Point out malaria parasites and leukocytes.
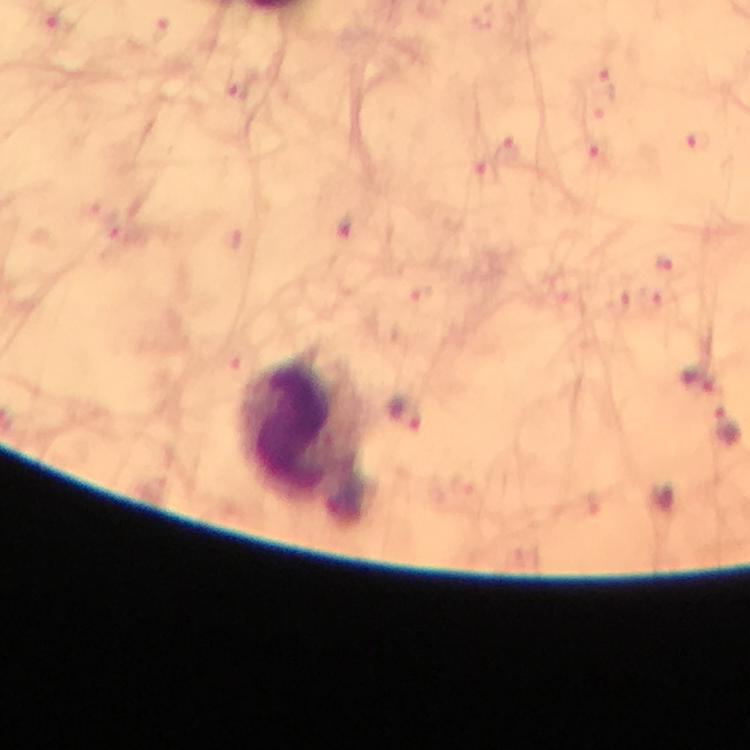

Approximate centers as (x, y) in pixels.
Malaria parasites: (698, 379), (404, 413), (728, 423).
Leukocytes: (310, 442).

preparation = thick blood smear
immersion oil = applied
magnification = 100x
context = from a diagnostic examination for malaria
cropped from = a single field of view
capture = smartphone camera through the microscope
image size = 750×750 pixels
stain = Giemsa